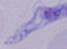
1000x magnification. Photomicrograph. A trypanosome is shown.